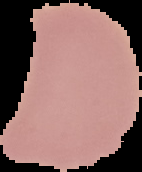
malaria_status: uninfected
image_type: cell region segmented out of the field of view; surrounding area masked to black
preparation: thin blood film
image_size: 142×172 pixels